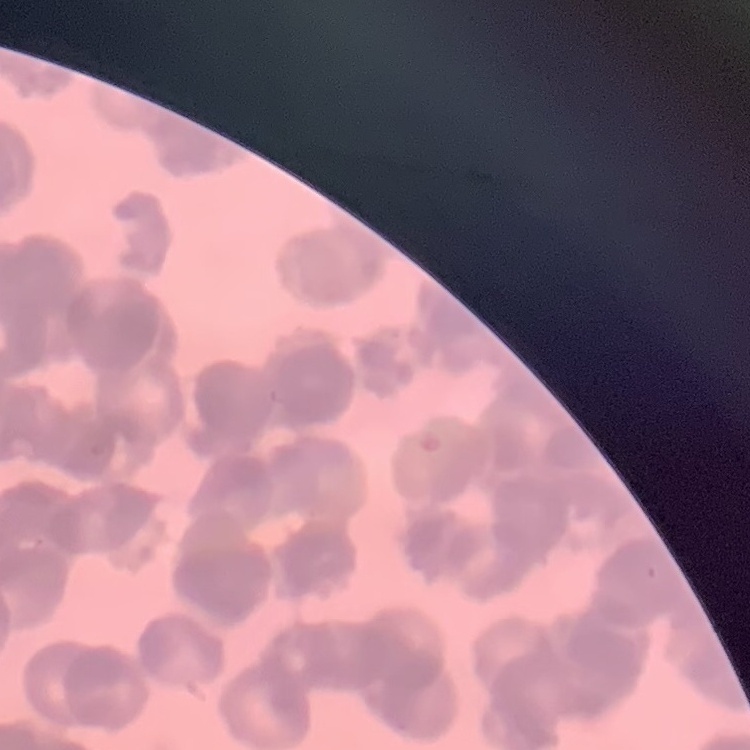
The erythrocytes show rouleaux formation. Stained with either Field's or Giemsa. One tile cut from a larger photomicrograph. Thin blood film.